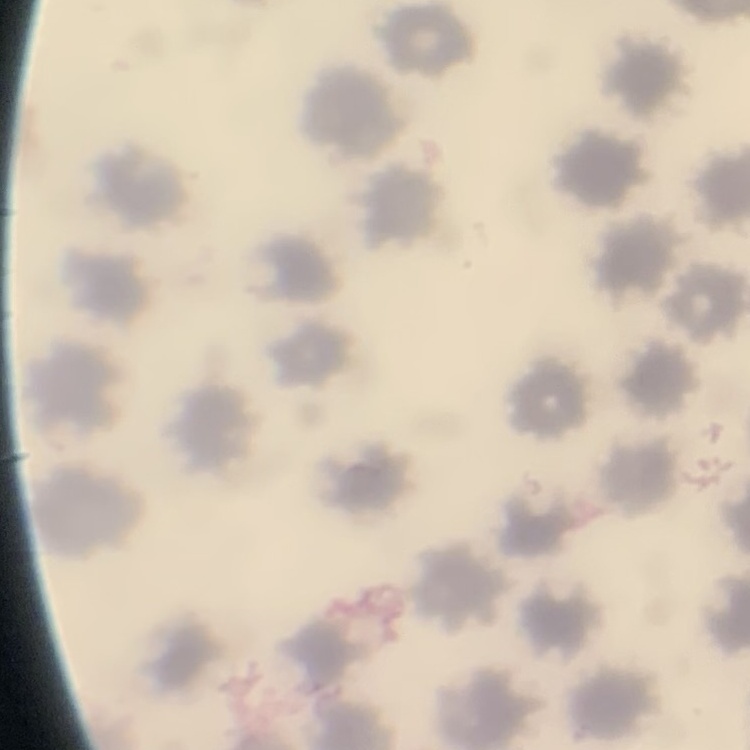 The red blood cells exhibit no rouleaux formation. Square crop of a larger photomicrograph. Thin peripheral smear. Stained with either Field's or Giemsa.